Name the parasite shown.
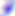

Toxoplasma gondii.

400x magnification. Micrograph.